Locate every malaria parasite.
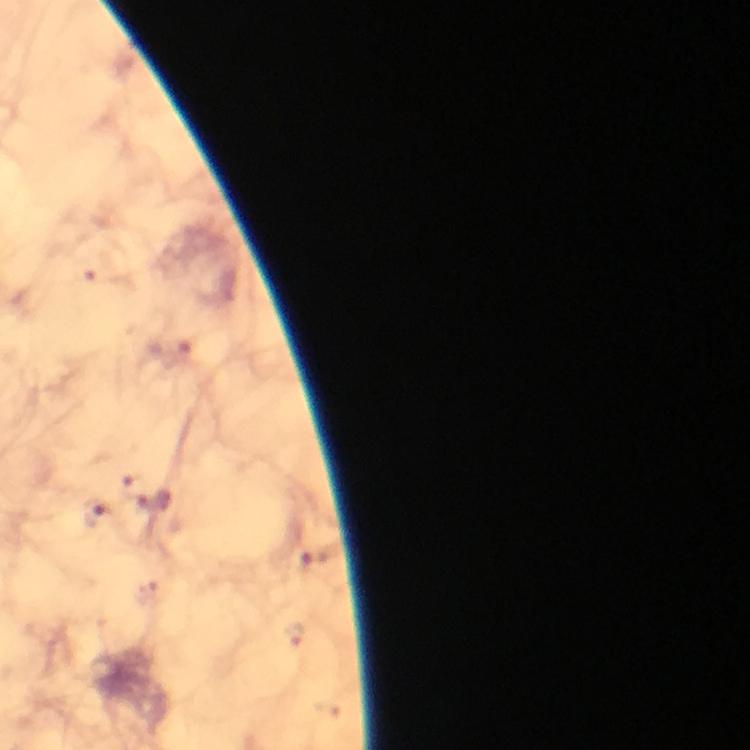

Approximate object centers, in pixels from the top-left corner.
Malaria parasites: (x=129, y=483), (x=157, y=505), (x=94, y=512), (x=316, y=561).

Cropped region of a single field of view. Photographed through the microscope with a smartphone camera. Immersion oil applied. Image is 750×750 pixels. Giemsa-stained preparation. At 100x magnification. From a malaria diagnostic workup. Thick smear.